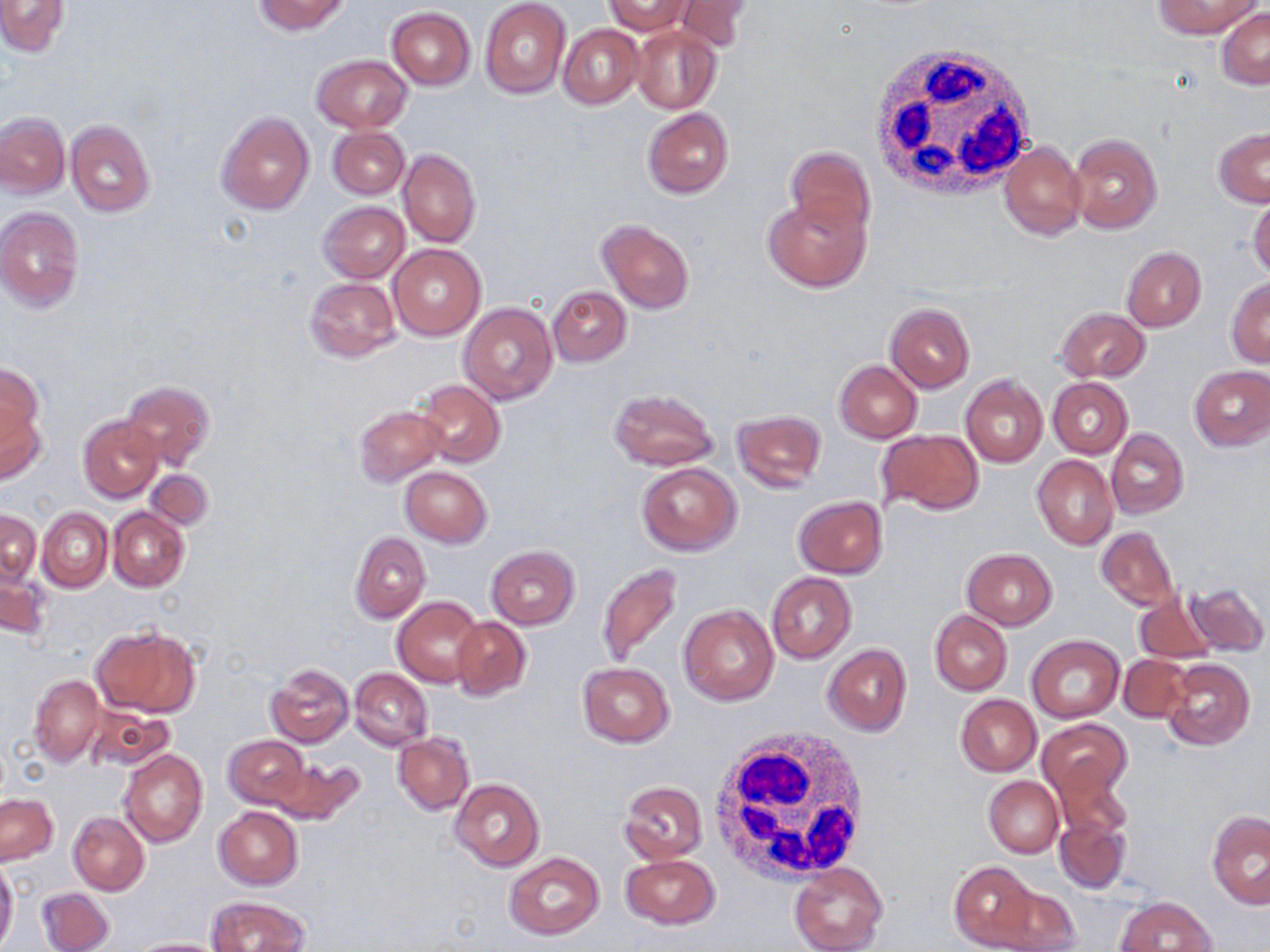
Approximate bounding boxes as (x1,y1)-(x2,y2) corner pairs in pixels. Uninfected red blood cell locations: (253,0)-(351,35), (479,0)-(570,99), (604,0)-(693,35), (670,0)-(755,52), (1154,0)-(1260,38), (0,1)-(68,55), (387,7)-(475,89), (1217,8)-(1270,89), (560,25)-(643,108), (631,26)-(722,113), (312,55)-(411,132), (642,107)-(735,199), (216,111)-(314,216), (0,114)-(69,198), (65,120)-(156,217), (1212,125)-(1270,207), (328,126)-(408,199), (1068,132)-(1163,235), (999,142)-(1086,240), (785,146)-(875,238), (397,149)-(482,248), (763,192)-(871,292), (1248,192)-(1270,281), (317,200)-(410,283), (0,207)-(84,313), (596,218)-(695,314), (389,242)-(487,341), (1121,246)-(1206,333), (304,276)-(401,361), (1226,277)-(1270,367), (547,285)-(631,366), (460,302)-(557,405), (886,303)-(975,392), (1056,308)-(1149,382), (834,360)-(921,443), (1,365)-(45,450), (1190,365)-(1270,450), (960,374)-(1048,468), (1048,377)-(1133,458), (120,379)-(215,472), (417,380)-(505,468), (608,388)-(719,471), (0,394)-(47,488), (353,405)-(445,486), (733,410)-(827,494), (78,415)-(164,503), (875,429)-(984,516), (1107,429)-(1189,518), (1032,455)-(1118,550), (638,462)-(742,555), (401,466)-(492,547), (145,468)-(215,530), (793,495)-(888,578), (37,507)-(113,592), (108,507)-(190,592), (1,509)-(41,587), (1095,527)-(1179,612), (350,531)-(430,623), (485,546)-(580,629), (962,548)-(1058,629), (597,562)-(684,670), (0,570)-(50,642), (766,573)-(856,663), (1187,581)-(1267,657), (1133,591)-(1216,665), (393,596)-(485,688), (678,604)-(779,705), (931,611)-(1011,696), (451,617)-(531,701), (92,625)-(202,717), (1026,635)-(1124,722), (823,643)-(912,736), (1119,654)-(1193,722), (1162,659)-(1254,750), (576,661)-(675,747), (266,664)-(354,747), (350,668)-(432,750), (29,674)-(105,767), (955,694)-(1041,775), (84,703)-(172,773), (1038,719)-(1132,801), (394,733)-(474,815), (223,735)-(309,811), (119,749)-(207,848), (266,756)-(362,826), (1051,756)-(1132,842), (984,776)-(1063,858), (451,778)-(545,872), (619,781)-(708,864), (1,794)-(56,865), (213,806)-(304,889), (1207,811)-(1270,909), (67,812)-(149,896), (1054,815)-(1130,895), (504,852)-(604,940), (620,854)-(721,930), (0,859)-(18,951), (948,861)-(1039,950), (788,862)-(887,952), (989,882)-(1081,951), (37,886)-(115,952), (206,896)-(309,951), (1117,896)-(1216,952), (129,938)-(230,951). White blood cell locations: (871,44)-(1039,199), (705,727)-(872,887). Slide-level diagnosis: negative for blood parasites. Image is 1270×952 pixels. One field of a larger specimen. Captured at 1000x magnification. May-Grünwald-Giemsa stain. Light microscopy. Thin blood smear.